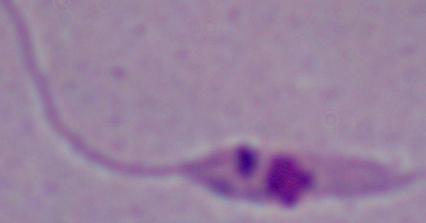

modality = micrograph
identification = Leishmania
magnification = 1000x